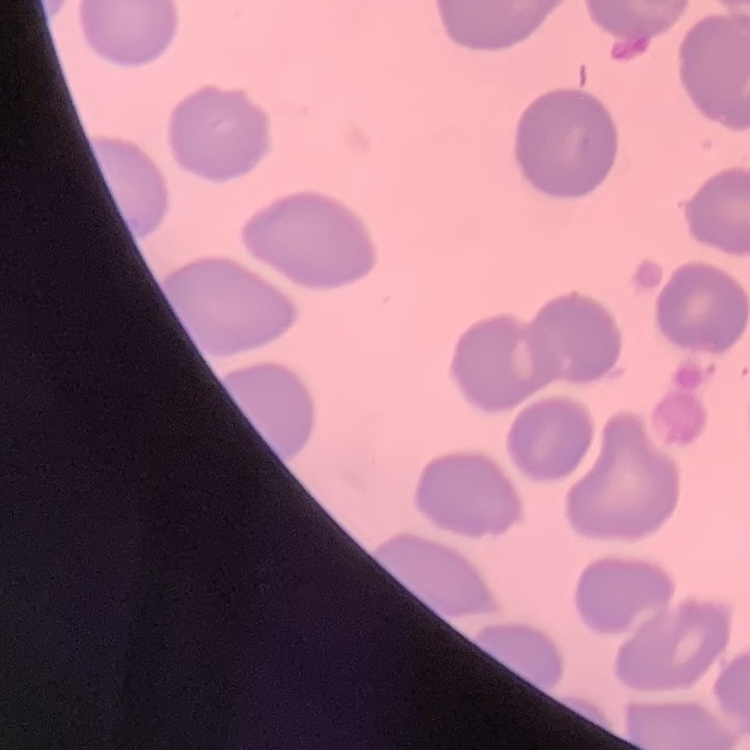

The erythrocytes exhibit no rouleaux formation. Square crop of a larger photomicrograph. Thin blood film. Field's or Giemsa stain.